Identify the preparation type.
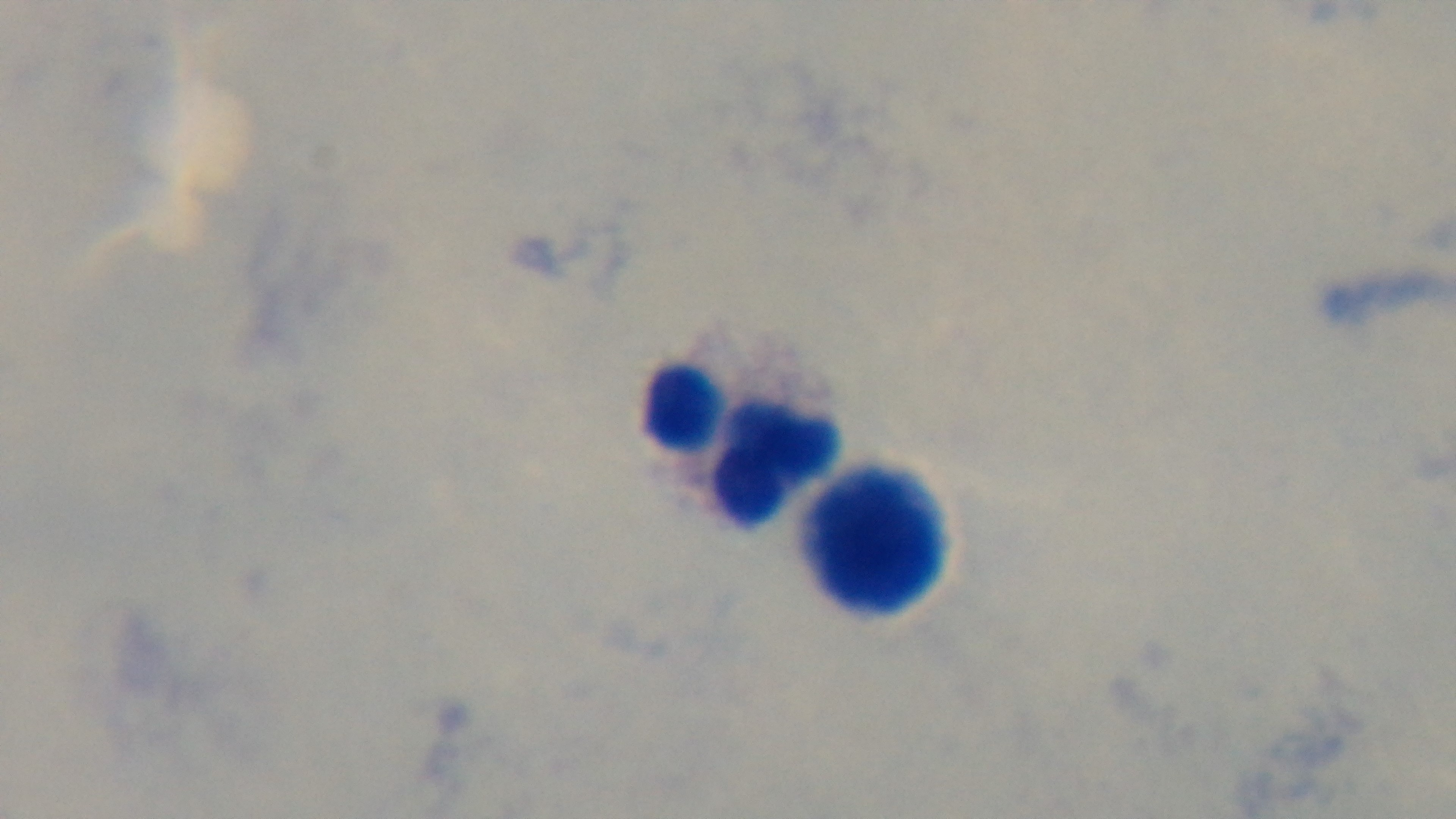
Thick.

modality = light microscopy
capture = mounted 4K digital camera
field of view = one from the slide
malaria status = uninfected
objective = 100x oil immersion
stain = Giemsa